State the blood parasite species.
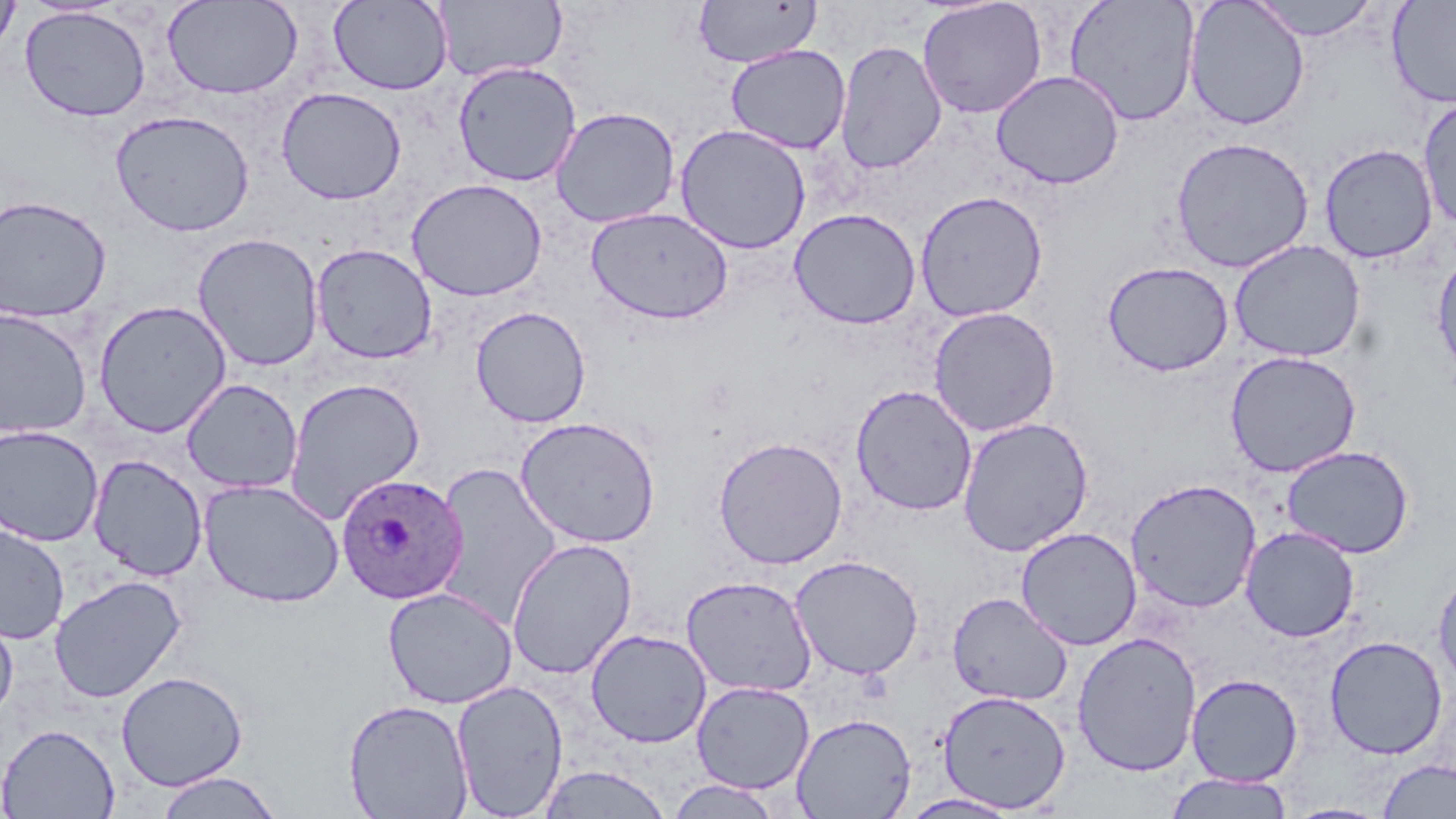

Plasmodium ovale.

{
  "field_of_view": "single",
  "uninfected_red_blood_cell_locations": "approximate bounding boxes as named x1/y1/x2/y2 corners in pixels: (x1=0, y1=0, x2=20, y2=60), (x1=162, y1=0, x2=303, y2=99), (x1=328, y1=0, x2=453, y2=94), (x1=694, y1=0, x2=822, y2=68), (x1=917, y1=0, x2=1047, y2=119), (x1=1064, y1=0, x2=1201, y2=127), (x1=1184, y1=0, x2=1310, y2=130), (x1=1247, y1=0, x2=1382, y2=41), (x1=1386, y1=0, x2=1456, y2=109), (x1=434, y1=1, x2=566, y2=80), (x1=20, y1=6, x2=151, y2=122), (x1=834, y1=39, x2=947, y2=175), (x1=725, y1=44, x2=851, y2=154), (x1=452, y1=61, x2=582, y2=187), (x1=990, y1=69, x2=1125, y2=189), (x1=276, y1=87, x2=407, y2=205), (x1=1417, y1=96, x2=1456, y2=231), (x1=549, y1=106, x2=681, y2=228), (x1=110, y1=110, x2=254, y2=236), (x1=674, y1=124, x2=812, y2=255), (x1=1170, y1=136, x2=1314, y2=273), (x1=1319, y1=143, x2=1438, y2=263), (x1=406, y1=178, x2=548, y2=302), (x1=914, y1=190, x2=1049, y2=322), (x1=0, y1=195, x2=112, y2=322), (x1=586, y1=207, x2=735, y2=324), (x1=788, y1=207, x2=922, y2=329), (x1=192, y1=232, x2=325, y2=372), (x1=1229, y1=239, x2=1366, y2=362), (x1=311, y1=243, x2=438, y2=364), (x1=1431, y1=249, x2=1456, y2=382), (x1=1101, y1=260, x2=1234, y2=377), (x1=94, y1=300, x2=231, y2=437), (x1=470, y1=305, x2=591, y2=428), (x1=928, y1=306, x2=1061, y2=437), (x1=0, y1=307, x2=94, y2=439), (x1=1224, y1=350, x2=1362, y2=477), (x1=181, y1=377, x2=303, y2=494), (x1=283, y1=377, x2=426, y2=523), (x1=850, y1=384, x2=978, y2=516), (x1=515, y1=415, x2=662, y2=548), (x1=956, y1=416, x2=1094, y2=557), (x1=0, y1=424, x2=104, y2=547), (x1=713, y1=436, x2=848, y2=569), (x1=1280, y1=445, x2=1415, y2=558), (x1=88, y1=454, x2=208, y2=581), (x1=431, y1=461, x2=562, y2=629), (x1=198, y1=478, x2=345, y2=608), (x1=1125, y1=478, x2=1261, y2=613), (x1=0, y1=523, x2=70, y2=644), (x1=1015, y1=526, x2=1143, y2=651), (x1=1240, y1=526, x2=1360, y2=642), (x1=506, y1=537, x2=637, y2=679), (x1=789, y1=554, x2=925, y2=680), (x1=1432, y1=565, x2=1456, y2=693), (x1=49, y1=575, x2=186, y2=704), (x1=680, y1=575, x2=818, y2=697), (x1=383, y1=587, x2=517, y2=709), (x1=947, y1=592, x2=1073, y2=706), (x1=0, y1=607, x2=18, y2=725), (x1=586, y1=628, x2=713, y2=748), (x1=1072, y1=631, x2=1202, y2=777), (x1=1324, y1=635, x2=1448, y2=759), (x1=116, y1=671, x2=248, y2=791), (x1=1186, y1=673, x2=1303, y2=786), (x1=451, y1=679, x2=568, y2=818), (x1=691, y1=681, x2=815, y2=794), (x1=938, y1=689, x2=1071, y2=812), (x1=343, y1=699, x2=474, y2=818), (x1=791, y1=713, x2=916, y2=819), (x1=1, y1=724, x2=120, y2=819), (x1=1377, y1=758, x2=1456, y2=818), (x1=536, y1=765, x2=674, y2=819), (x1=153, y1=771, x2=284, y2=819), (x1=1164, y1=773, x2=1294, y2=818), (x1=664, y1=778, x2=786, y2=818), (x1=899, y1=792, x2=1023, y2=818), (x1=1282, y1=802, x2=1393, y2=819)",
  "stain": "May-Grünwald-Giemsa",
  "magnification": "1000x",
  "preparation": "thin blood film",
  "plasmodium_ovale_infected_red_blood_cell_locations": "approximate bounding boxes as named x1/y1/x2/y2 corners in pixels: (x1=334, y1=473, x2=468, y2=604)",
  "image_size": "1456×819 pixels",
  "modality": "optical microscopy"
}